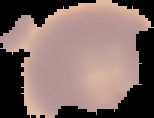

Summary:
  - Preparation: thin blood smear
  - Image type: segmented cell region on a black background
  - Malaria status: uninfected
  - Image size: 154×118 pixels